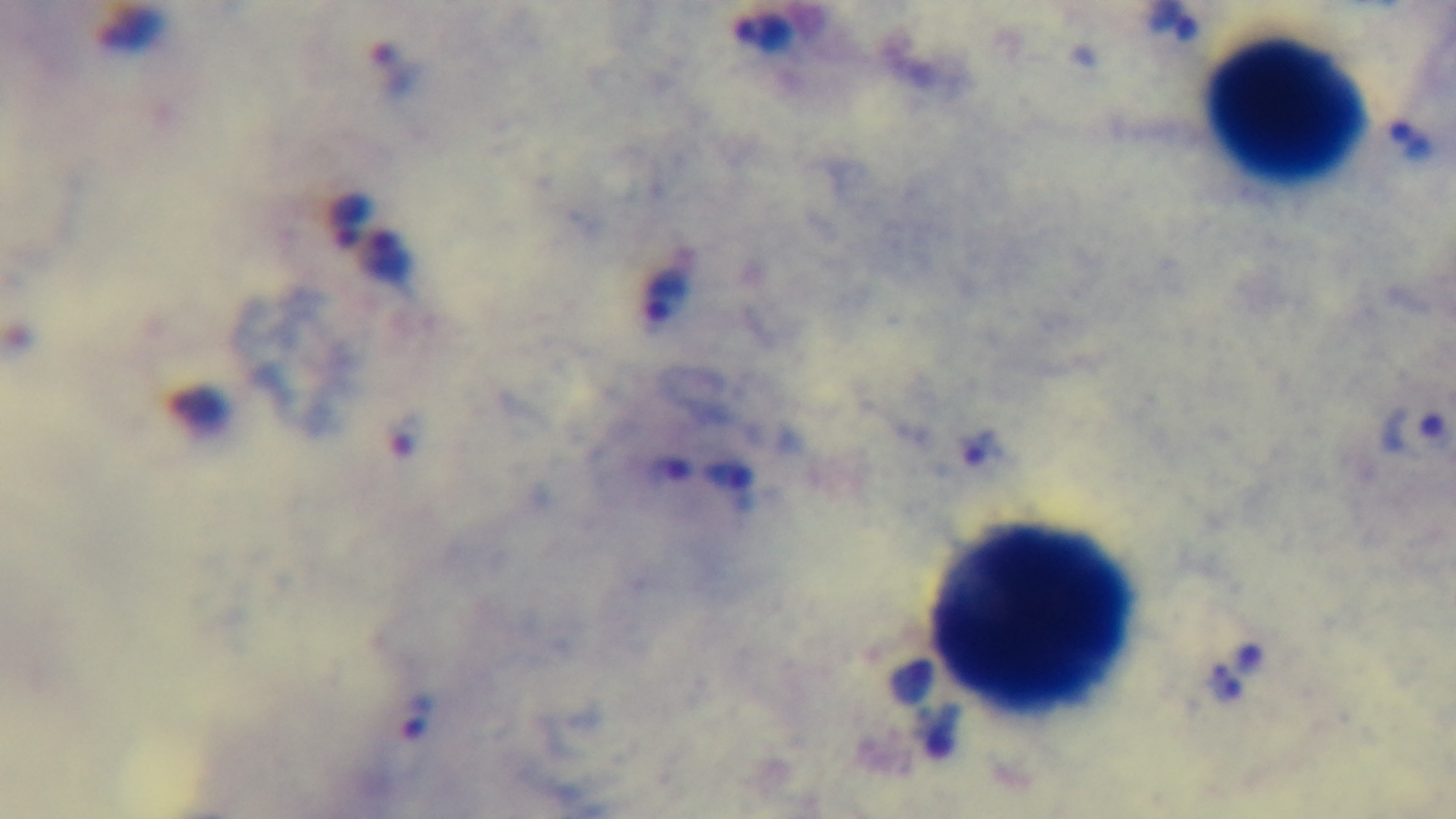

Summary:
  - Objective: 100x oil immersion
  - Capture: mounted 4K digital camera
  - Stain: Giemsa
  - Malaria status: positive
  - Field of view: single
  - Modality: light microscopy
  - Preparation: thick blood film